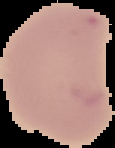

image size = 115×148 pixels
malaria status = uninfected
preparation = thin blood smear
image type = segmented cell region on a black background